State the preparation type.
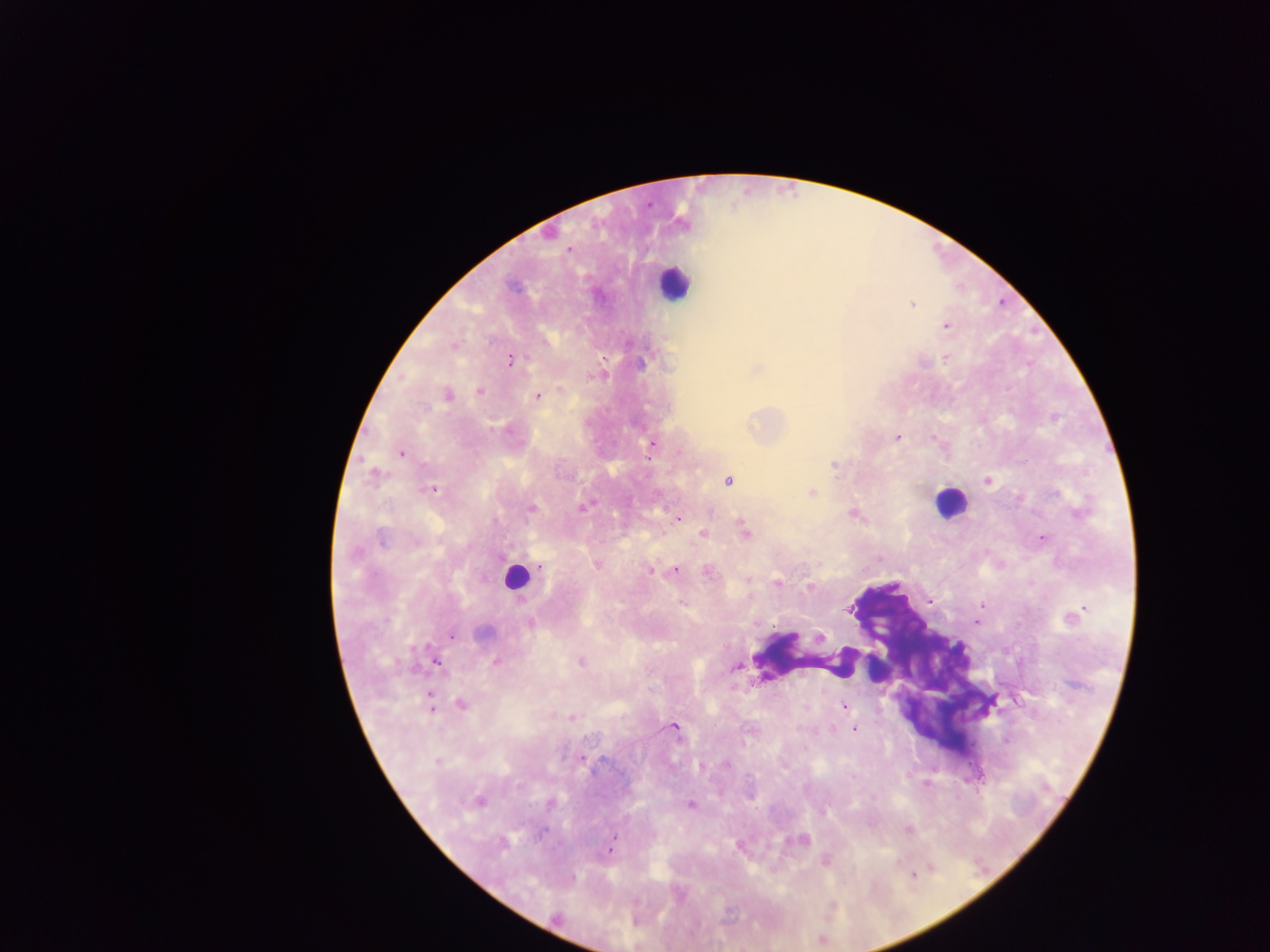

Thick blood smear.

{
  "field_of_view": "single",
  "country": "Ghana",
  "leukocyte_locations": "approximate centers as [x, y] in pixels: [674, 282], [950, 502], [516, 577], [809, 656], [879, 665]",
  "image_size": "1270×952 pixels",
  "malaria_parasite_locations": "approximate centers as [x, y] in pixels: [570, 249], [912, 304], [946, 326], [946, 359], [510, 360], [640, 363], [757, 368], [561, 389], [480, 390], [447, 395], [537, 396], [424, 408], [897, 437], [934, 437], [651, 446], [401, 453], [834, 466], [375, 476], [988, 480], [728, 481], [433, 489], [812, 492], [582, 507], [531, 508], [853, 514], [678, 518], [745, 530], [703, 533], [1042, 538], [382, 539], [355, 554], [596, 565], [540, 567], [675, 570], [650, 571], [708, 571], [748, 579], [777, 583], [809, 587], [682, 603], [982, 606], [1077, 613], [530, 624], [483, 632], [452, 636], [820, 637], [435, 661], [581, 661], [496, 662], [736, 667], [431, 702], [462, 705], [843, 707], [572, 718], [675, 728], [854, 729], [582, 759], [436, 761], [727, 765], [478, 801], [550, 803], [690, 805], [908, 830], [801, 840], [504, 843], [611, 846], [826, 861], [913, 875]",
  "capture": "mobile-phone photograph through a microscope"
}